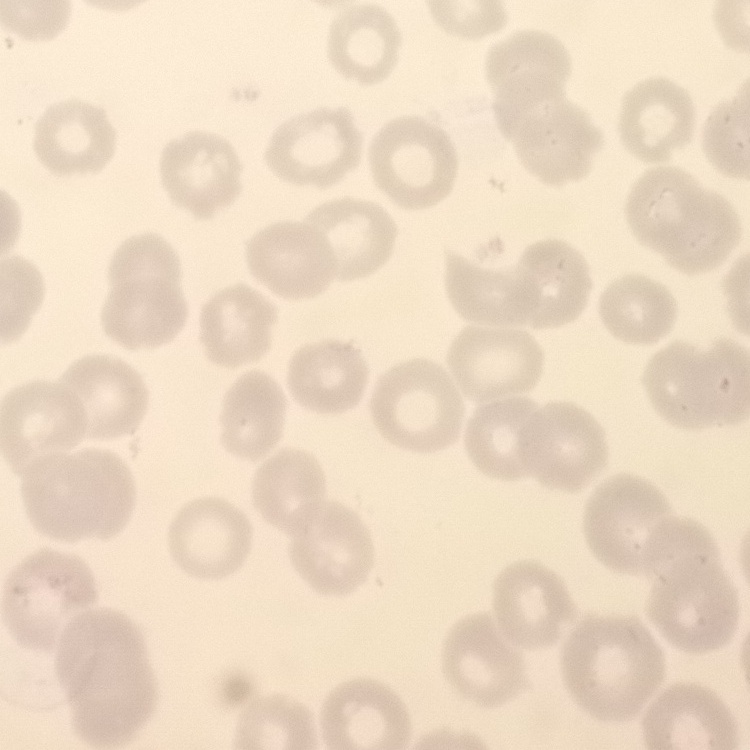

erythrocyte_morphology: no rouleaux formation
stain: Field's or Giemsa
image_type: square crop of a larger photomicrograph
preparation: thin blood smear